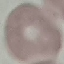
Malaria status: uninfected. Thin blood film. Automatically extracted cell patch, resized to 64 × 64 pixels. Photographed with a smartphone camera at the microscope eyepiece. Giemsa stain.